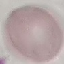 Malaria status: uninfected. Cell patch, automatically extracted from a larger field of view and resized to 64 × 64 pixels. Giemsa-stained preparation. Photographed with a smartphone camera at the microscope eyepiece. Thin blood smear.